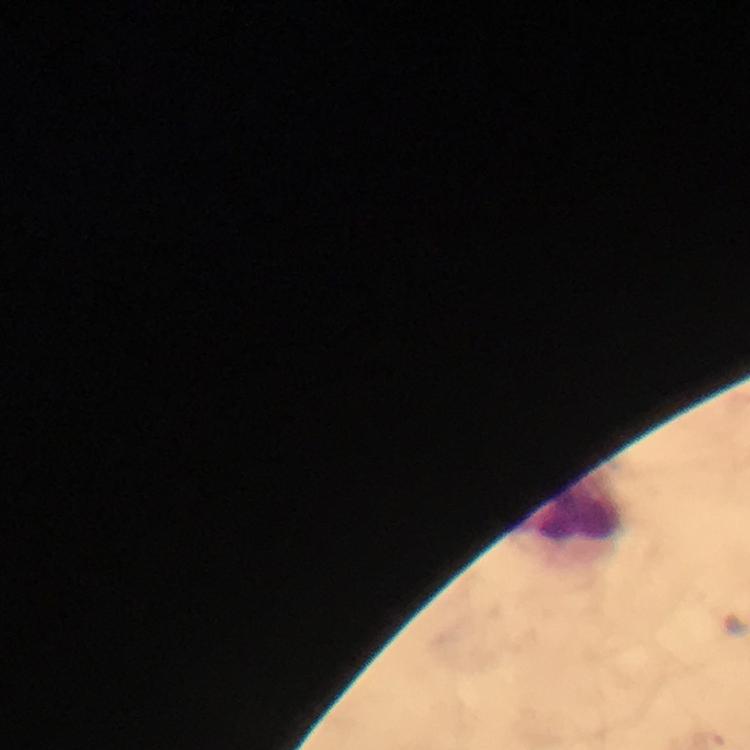
Approximate centers as [x, y] in pixels. Leukocyte locations: [577, 508]. Giemsa stain. Smartphone photograph taken through a microscope. Malaria parasites: none detected. Cropped region of a single field of view. Thick blood film. At 100x magnification. Image is 750×750 pixels. Immersion oil applied. From a diagnostic examination for malaria.